Classify this cell by malaria status.
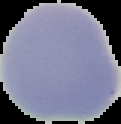

It is uninfected.

preparation = thin blood film
image type = segmented cell region on a black background
image size = 121×124 pixels